Identify the parasite.
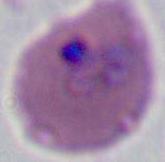
Plasmodium.

400x or 1000x magnification. Photomicrograph.